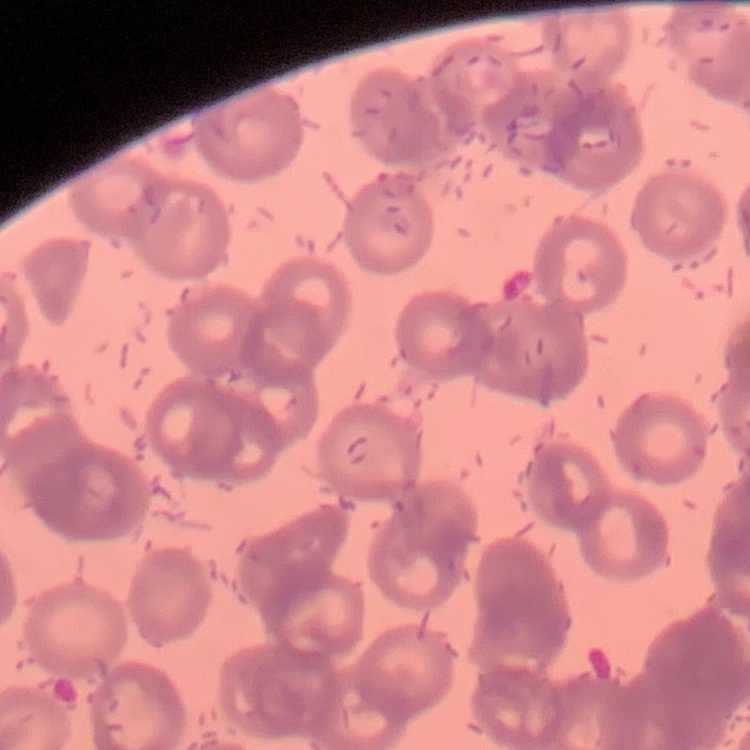

The erythrocytes exhibit rouleaux formation. Stained with either Field's or Giemsa. Thin peripheral smear. Square crop of a larger photomicrograph.